Locate every leukocyte (white blood cell).
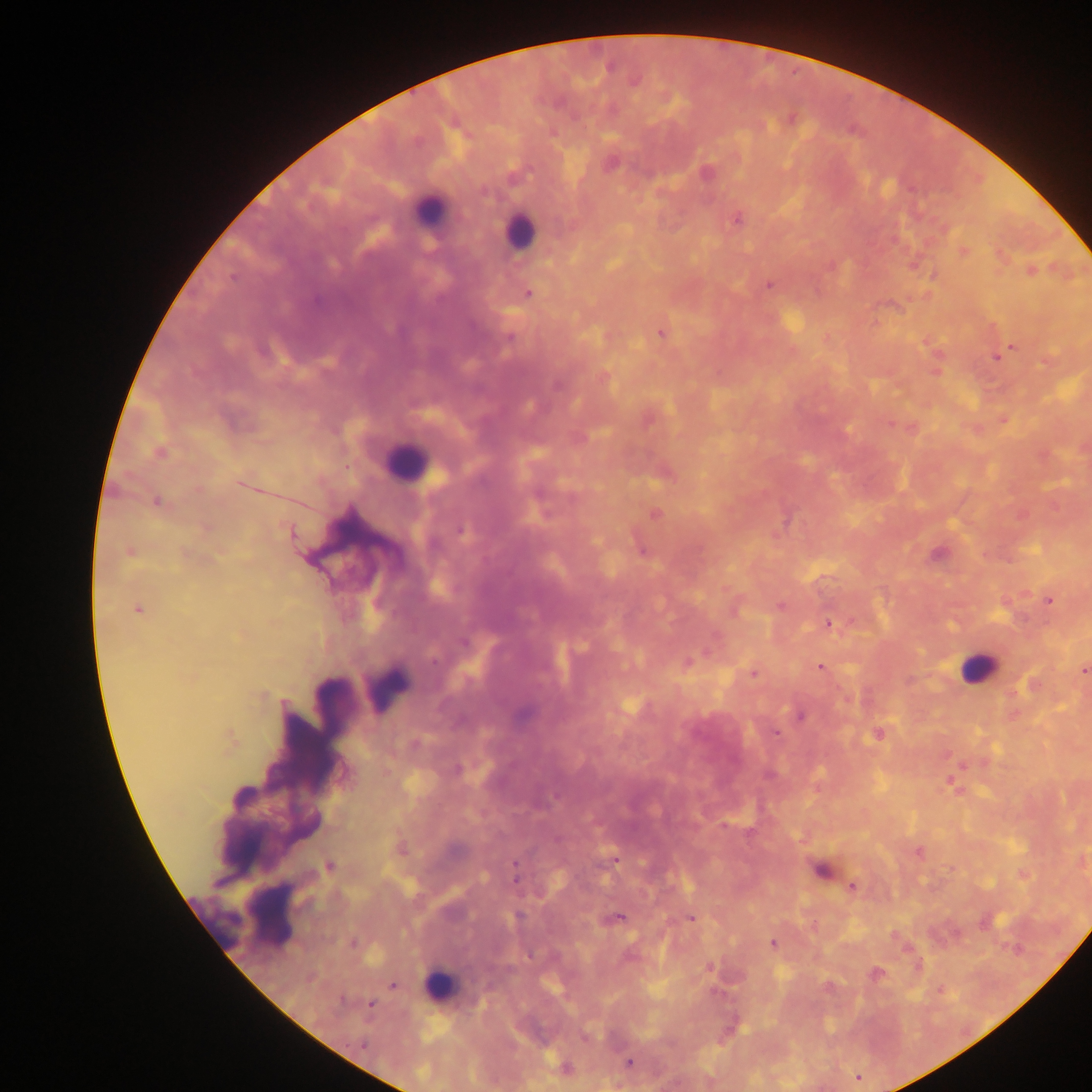

Approximate centers as (x, y) in pixels.
Leukocytes: (428, 211), (519, 231), (405, 463), (977, 668), (388, 686), (214, 914), (274, 914), (441, 984).

Summary:
  - Malaria parasite locations: (634, 82), (706, 173), (484, 190), (737, 219), (964, 251), (1031, 271), (768, 285), (528, 293), (661, 334), (509, 337), (1012, 347), (997, 356), (557, 385), (890, 425), (159, 452), (240, 485), (157, 502), (654, 513), (461, 529), (291, 533), (642, 551), (129, 552), (938, 554), (1049, 601), (781, 606), (138, 609), (828, 623), (463, 643), (434, 659), (687, 663), (820, 668), (1084, 671), (753, 674), (801, 716), (776, 734), (877, 734), (229, 739), (724, 826), (919, 853), (615, 860), (329, 866), (820, 870), (515, 876), (852, 886), (518, 916), (619, 917), (691, 918), (353, 942), (772, 943), (1016, 949), (530, 954), (709, 968), (875, 974), (393, 985), (341, 1001), (370, 1005), (363, 1044), (629, 1063), (566, 1068), (857, 1078)
  - Image size: 1092×1092 pixels
  - Preparation: thick blood film
  - Field of view: single
  - Country: Ghana
  - Capture: mobile-phone photograph through a microscope